Classify this cell by malaria status.
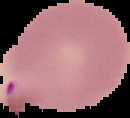

It is parasitized.

From a thin blood film. The area outside the segmented cell region is set to black. Image is 130×118 pixels.